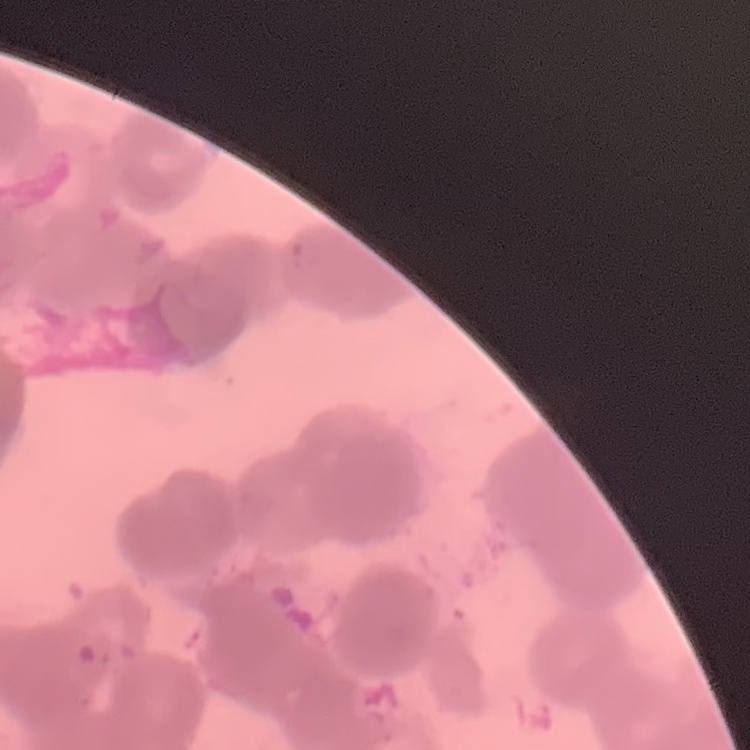
Summary:
  - Erythrocyte morphology: rouleaux formation
  - Stain: Field's or Giemsa
  - Preparation: thin blood film
  - Image type: one tile cut from a larger photomicrograph